Name the cell type shown.
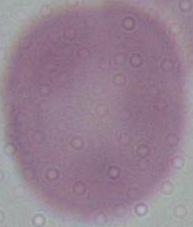

This is an erythrocyte.

Summary:
  - Modality: micrograph
  - Magnification: 1000x